Name the parasite shown.
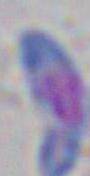
This is Toxoplasma gondii.

modality = micrograph
magnification = 1000x